Locate every malaria parasite.
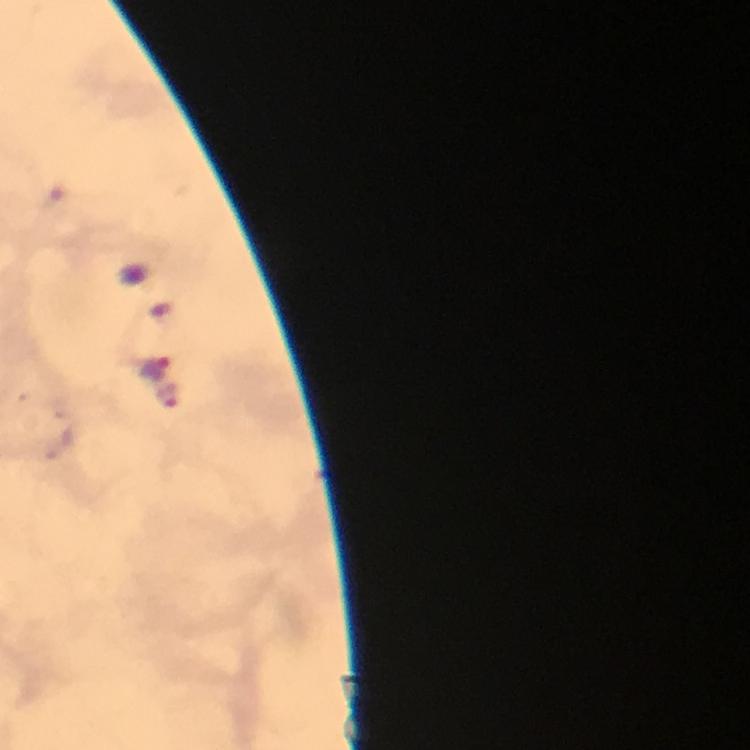

Approximate object centers, in pixels from the top-left corner.
Malaria parasites: (x=153, y=368), (x=169, y=396).

Summary:
  - Cropped from: one field of view
  - Stain: Giemsa
  - Context: from a malaria diagnostic workup
  - Immersion oil: applied
  - Image size: 750×750 pixels
  - Magnification: 100x
  - Capture: smartphone mounted on the microscope
  - Preparation: thick blood smear